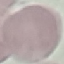
malaria_status: uninfected
preparation: thin blood smear
image_type: cell patch, automatically extracted from a larger field of view and resized to 64 × 64 pixels
stain: Giemsa
capture: smartphone through the microscope eyepiece